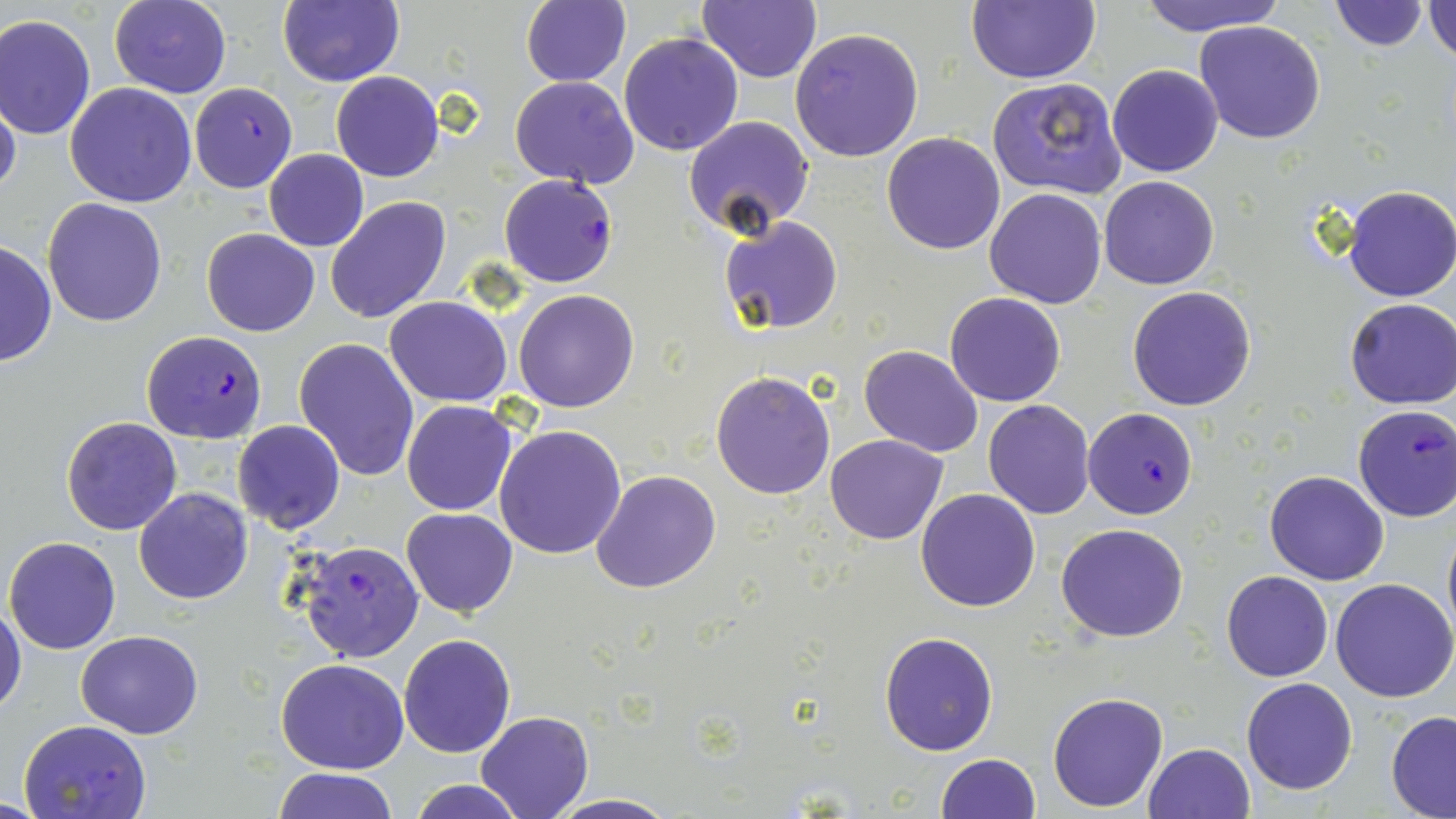

slide-level diagnosis = Plasmodium falciparum
field of view = single
modality = optical microscopy
image size = 1456×819 pixels
stain = May-Grünwald-Giemsa
uninfected red blood cell locations = approximate bounding boxes as named x1/y1/x2/y2 corners in pixels: (x1=107, y1=0, x2=232, y2=99), (x1=277, y1=0, x2=403, y2=87), (x1=520, y1=0, x2=630, y2=86), (x1=697, y1=0, x2=820, y2=82), (x1=966, y1=0, x2=1098, y2=85), (x1=1133, y1=0, x2=1287, y2=37), (x1=1330, y1=0, x2=1431, y2=51), (x1=1424, y1=1, x2=1456, y2=62), (x1=0, y1=14, x2=97, y2=140), (x1=1193, y1=20, x2=1327, y2=144), (x1=792, y1=27, x2=924, y2=162), (x1=619, y1=33, x2=744, y2=157), (x1=1107, y1=64, x2=1224, y2=178), (x1=330, y1=70, x2=444, y2=182), (x1=511, y1=76, x2=640, y2=188), (x1=987, y1=76, x2=1127, y2=200), (x1=65, y1=81, x2=198, y2=207), (x1=0, y1=88, x2=22, y2=205), (x1=683, y1=116, x2=816, y2=241), (x1=881, y1=132, x2=1006, y2=255), (x1=265, y1=149, x2=367, y2=251), (x1=1099, y1=175, x2=1220, y2=290), (x1=1340, y1=184, x2=1456, y2=302), (x1=986, y1=188, x2=1109, y2=309), (x1=43, y1=197, x2=167, y2=326), (x1=326, y1=197, x2=450, y2=323), (x1=718, y1=214, x2=842, y2=334), (x1=202, y1=228, x2=320, y2=338), (x1=0, y1=241, x2=56, y2=368), (x1=1127, y1=286, x2=1256, y2=411), (x1=513, y1=289, x2=640, y2=412), (x1=944, y1=292, x2=1068, y2=407), (x1=384, y1=296, x2=512, y2=405), (x1=1345, y1=298, x2=1456, y2=410), (x1=293, y1=337, x2=420, y2=480), (x1=859, y1=344, x2=984, y2=457), (x1=711, y1=372, x2=835, y2=499), (x1=983, y1=400, x2=1096, y2=519), (x1=402, y1=401, x2=517, y2=515), (x1=60, y1=417, x2=182, y2=536), (x1=231, y1=421, x2=345, y2=535), (x1=494, y1=424, x2=626, y2=559), (x1=825, y1=434, x2=947, y2=543), (x1=591, y1=469, x2=720, y2=593), (x1=1264, y1=471, x2=1389, y2=585), (x1=133, y1=487, x2=254, y2=604), (x1=915, y1=488, x2=1040, y2=612), (x1=401, y1=508, x2=518, y2=617), (x1=1441, y1=516, x2=1456, y2=645), (x1=1056, y1=523, x2=1188, y2=643), (x1=5, y1=537, x2=122, y2=656), (x1=1221, y1=570, x2=1334, y2=682), (x1=1331, y1=578, x2=1456, y2=702), (x1=1, y1=601, x2=26, y2=721), (x1=75, y1=630, x2=203, y2=739), (x1=879, y1=631, x2=999, y2=755), (x1=398, y1=634, x2=517, y2=757), (x1=276, y1=658, x2=408, y2=773), (x1=1241, y1=677, x2=1358, y2=795), (x1=1046, y1=691, x2=1168, y2=812), (x1=477, y1=710, x2=593, y2=819), (x1=1386, y1=711, x2=1456, y2=817), (x1=1143, y1=742, x2=1255, y2=819), (x1=936, y1=753, x2=1040, y2=818), (x1=271, y1=768, x2=399, y2=819), (x1=407, y1=778, x2=526, y2=819), (x1=542, y1=793, x2=680, y2=819)
Plasmodium falciparum-infected red blood cell locations = approximate bounding boxes as named x1/y1/x2/y2 corners in pixels: (x1=188, y1=83, x2=297, y2=192), (x1=499, y1=173, x2=618, y2=287), (x1=138, y1=332, x2=268, y2=464), (x1=1351, y1=404, x2=1456, y2=522), (x1=1083, y1=408, x2=1199, y2=518), (x1=299, y1=541, x2=425, y2=664), (x1=17, y1=719, x2=151, y2=818)
magnification = 1000x
preparation = thin blood film